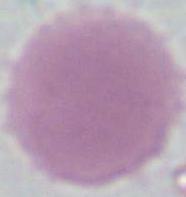
magnification: 1000x
modality: photomicrograph
identification: erythrocyte